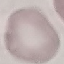
Malaria status: uninfected. Thin blood film. Photographed with a smartphone camera at the microscope eyepiece. Giemsa stain. Cell patch, automatically extracted from a larger field of view and resized to 64 × 64 pixels.